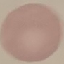
Summary:
  - Malaria status: uninfected
  - Preparation: thin smear
  - Stain: Giemsa
  - Capture: smartphone camera at the microscope eyepiece
  - Image type: automatically extracted cell patch, resized to 64 × 64 pixels